Identify the cell.
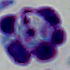

This is a leukocyte.

{
  "modality": "micrograph",
  "magnification": "1000x"
}